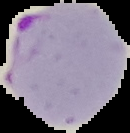
preparation = thin blood smear
image type = cell region segmented out of the field of view; surrounding area masked to black
malaria status = parasitized
image size = 130×133 pixels